Locate every leukocyte (white blood cell).
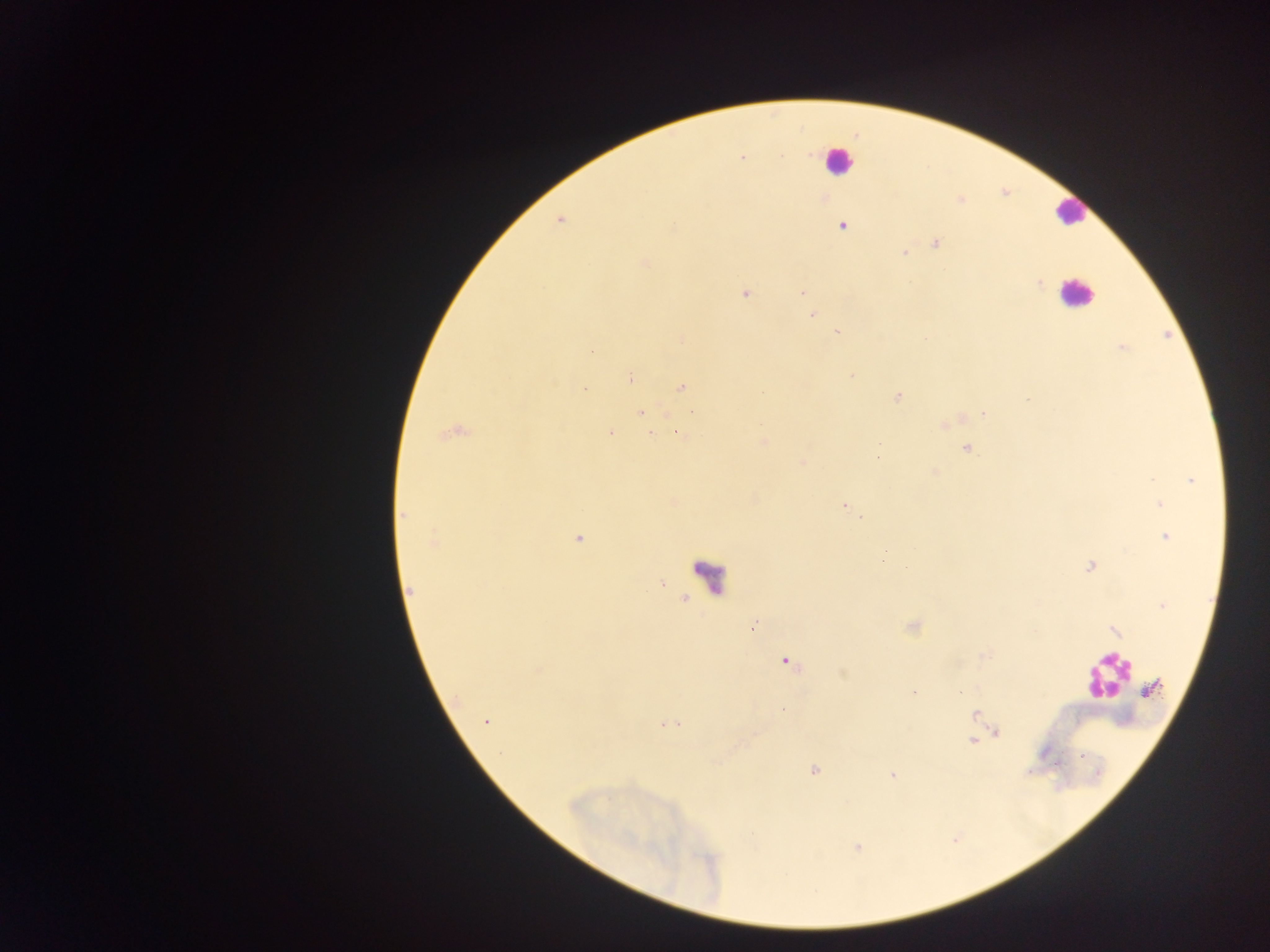
No leukocytes observed.

Approximate centers as x y in pixels.
Summary:
  - Malaria parasite locations: 783 156; 741 157; 824 198; 842 226; 934 243; 904 251; 645 263; 1038 282; 802 291; 743 294; 814 314; 836 330; 1122 347; 592 352; 850 375; 629 377; 553 383; 681 387; 584 390; 897 397; 1025 399; 692 410; 639 412; 983 413; 950 422; 944 424; 451 432; 611 433; 677 433; 650 434; 764 440; 965 448; 877 456; 802 463; 933 471; 1192 479; 1158 502; 845 503; 402 513; 862 519; 1164 535; 433 537; 578 538; 1088 565; 660 582; 411 590; 1163 606; 754 625; 912 626; 1116 632; 786 661; 842 674; 913 692; 784 710; 486 722; 678 723; 664 724; 673 726; 996 732; 972 741; 718 762; 814 770; 893 774; 750 835; 858 847
  - Preparation: thick blood film
  - Field of view: single
  - Image size: 1270×952 pixels
  - Capture: mobile-phone photograph through a microscope
  - Country: Ghana